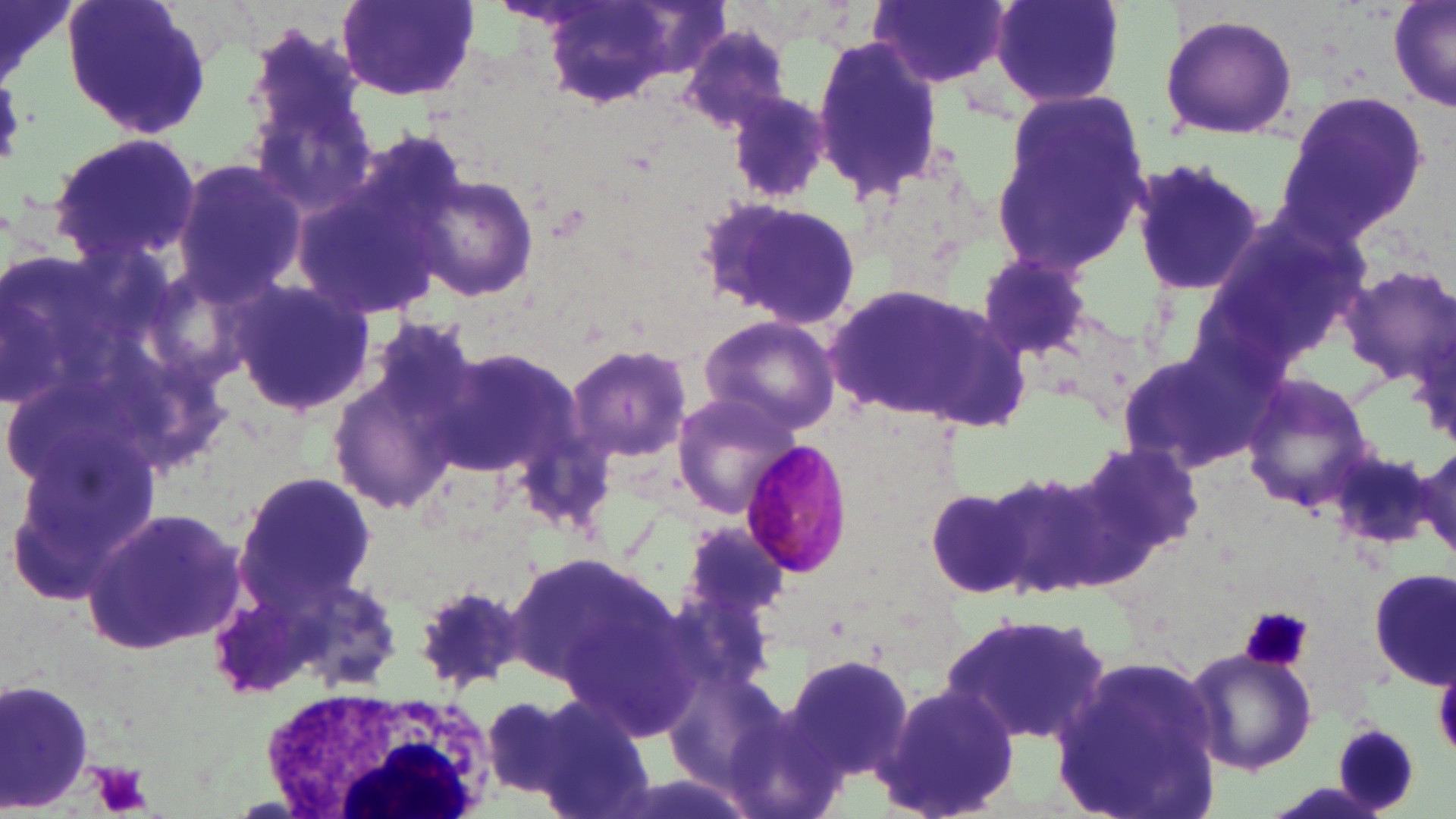

Summary:
  - Coordinate format: approximate bounding boxes as (x1,y1)-(x2,y2) corner pairs in pixels
  - Plasmodium malariae-infected red blood cell locations: (735,441)-(855,581)
  - White blood cell locations: (249,681)-(513,816)
  - Platelet locations: (1237,607)-(1314,672), (85,763)-(153,816)
  - Uninfected red blood cell locations: (1,0)-(78,88), (61,0)-(211,141), (868,0)-(1011,91), (984,0)-(1128,110), (336,1)-(481,102), (1388,1)-(1456,117), (539,4)-(726,112), (1157,11)-(1299,142), (677,23)-(798,135), (809,32)-(950,209), (720,87)-(837,206), (990,89)-(1150,276), (1277,91)-(1430,241), (43,129)-(205,269), (171,155)-(307,306), (1128,155)-(1267,300), (291,168)-(451,326), (411,175)-(536,300), (698,193)-(865,330), (1197,209)-(1367,361), (0,249)-(125,407), (975,253)-(1097,361), (1337,267)-(1456,387), (225,280)-(374,417), (823,283)-(1033,431), (696,313)-(843,438), (326,321)-(481,517), (429,343)-(585,486), (563,343)-(694,465), (1114,349)-(1260,475), (1237,372)-(1377,514), (671,390)-(807,519), (1074,438)-(1204,572), (5,439)-(154,612), (988,461)-(1138,599), (230,470)-(377,616), (924,486)-(1032,600), (79,507)-(247,654), (680,516)-(795,629), (504,548)-(666,695), (1370,567)-(1455,687), (295,576)-(403,694), (409,584)-(531,692), (941,612)-(1112,747), (1183,644)-(1318,776), (781,653)-(915,783), (1051,655)-(1225,819), (0,678)-(95,817), (876,680)-(1021,819), (477,692)-(595,805), (531,702)-(660,819)
  - Slide-level diagnosis: Plasmodium malariae
  - Magnification: 1000x
  - Image size: 1456×819 pixels
  - Preparation: thin blood film
  - Field of view: one of a larger specimen
  - Modality: optical microscopy
  - Stain: May-Grünwald-Giemsa